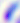
magnification = 400x
modality = photomicrograph
identification = Toxoplasma gondii